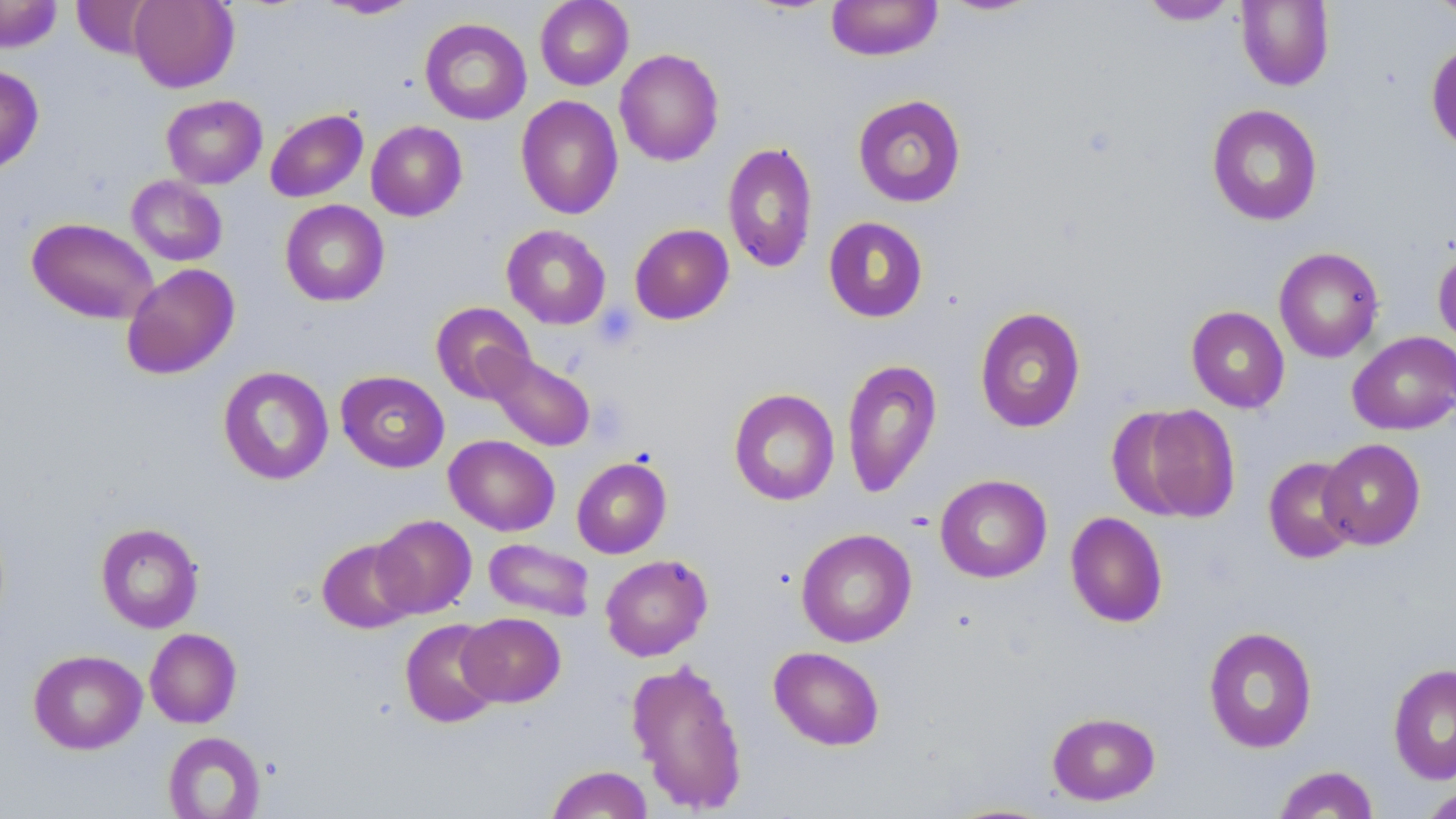
{
  "slide_level_diagnosis": "negative for blood parasites",
  "field_of_view": "single",
  "platelet_locations": "approximate bounding boxes as (x1,y1)-(x2,y2) corner pairs in pixels: (593,305)-(639,349)",
  "modality": "light microscopy",
  "uninfected_red_blood_cell_locations": "approximate bounding boxes as (x1,y1)-(x2,y2) corner pairs in pixels: (0,0)-(62,53), (72,0)-(157,58), (128,0)-(239,93), (316,0)-(421,20), (535,0)-(633,90), (827,0)-(943,61), (1139,0)-(1239,25), (1427,0)-(1456,24), (936,1)-(1045,17), (1236,1)-(1335,91), (420,18)-(532,125), (1426,40)-(1456,155), (614,48)-(724,167), (0,64)-(44,175), (852,94)-(967,208), (161,95)-(267,189), (515,95)-(624,220), (1206,104)-(1323,226), (265,108)-(368,202), (366,120)-(467,221), (722,140)-(818,274), (126,175)-(227,266), (280,200)-(389,306), (26,217)-(159,324), (823,217)-(928,323), (629,223)-(734,325), (501,224)-(612,329), (1433,246)-(1456,352), (1274,247)-(1384,363), (121,263)-(240,379), (430,302)-(536,404), (974,305)-(1086,433), (1186,306)-(1290,413), (1347,331)-(1456,435), (485,353)-(595,451), (842,358)-(942,498), (218,365)-(334,485), (335,370)-(450,473), (728,388)-(840,506), (1112,403)-(1242,523), (444,434)-(560,536), (1318,438)-(1426,550), (572,456)-(672,559), (1263,457)-(1361,564), (935,474)-(1052,583), (1065,511)-(1168,628), (372,515)-(477,618), (95,522)-(204,633), (795,528)-(917,648), (317,538)-(419,634), (483,538)-(595,622), (600,554)-(713,661), (458,612)-(565,707), (399,618)-(503,728), (1203,625)-(1318,753), (145,628)-(242,728), (768,646)-(885,751), (28,649)-(147,754), (625,657)-(749,814), (1388,662)-(1456,785), (1047,711)-(1160,806), (162,731)-(266,819), (1272,764)-(1380,818), (546,765)-(653,818), (1420,786)-(1456,819)",
  "stain": "May-Grünwald-Giemsa",
  "magnification": "1000x",
  "preparation": "thin blood film",
  "image_size": "1456×819 pixels"
}